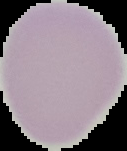
From a thin blood film. Segmented cell region on a black background. Result: negative for malaria parasites. Image is 127×151 pixels.